Locate every blood parasite and identify its species.
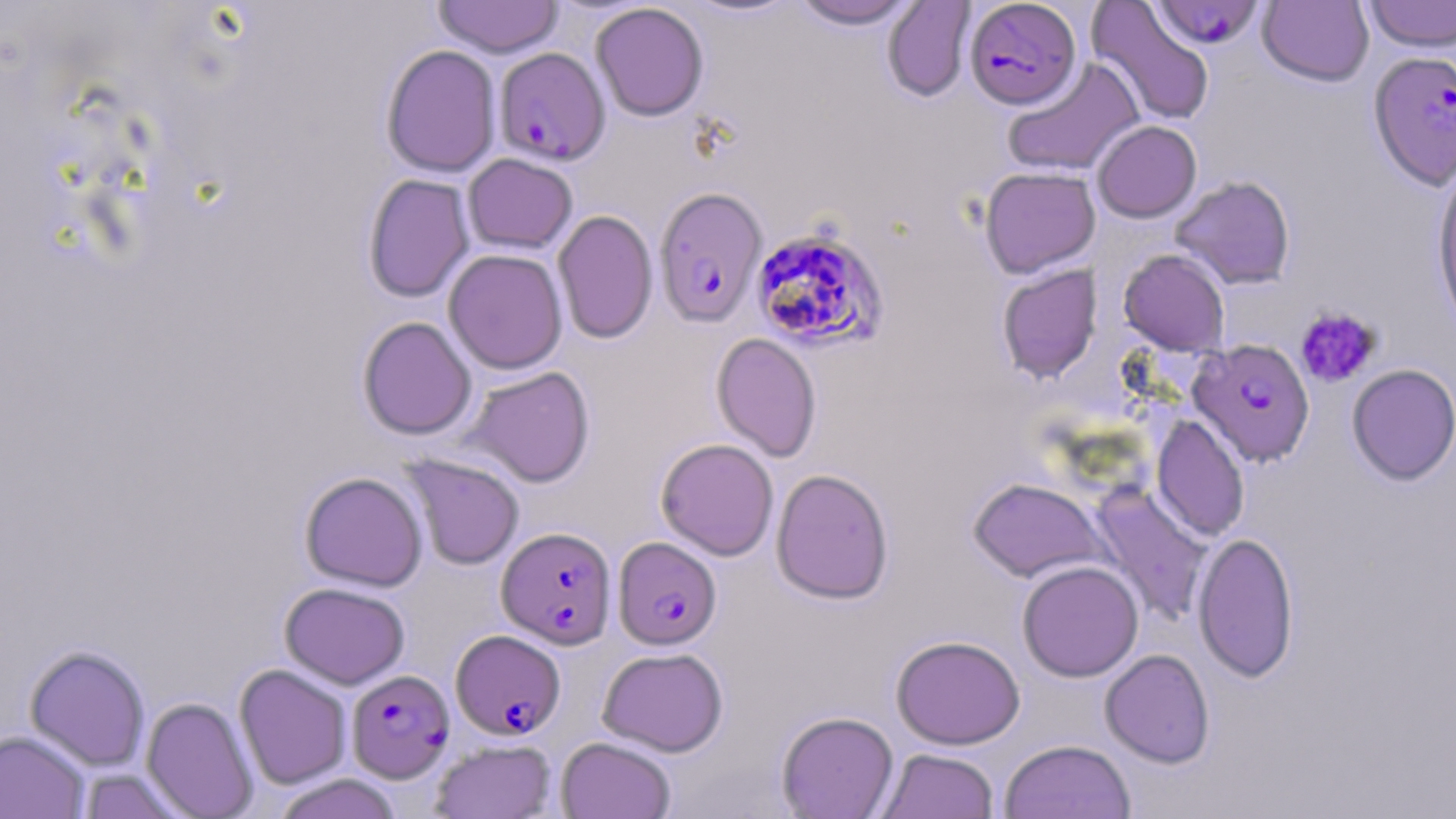
Approximate bounding boxes as [x1, y1, x2, y2] in pixels.
Plasmodium falciparum-infected red blood cells: [965, 0, 1081, 109], [1151, 1, 1264, 48], [494, 47, 610, 166], [1368, 50, 1456, 191], [653, 186, 768, 328], [751, 228, 888, 352], [1189, 338, 1315, 467], [497, 526, 617, 648], [613, 536, 721, 650], [450, 629, 565, 740], [346, 669, 454, 783].
No Plasmodium ovale, Plasmodium malariae, Plasmodium vivax, Babesia divergens, or Trypanosoma brucei observed.

Platelet locations: [1296, 306, 1382, 388]. Uninfected red blood cell locations: [678, 0, 806, 20], [790, 0, 920, 29], [1087, 0, 1215, 126], [1361, 0, 1456, 52], [433, 1, 564, 58], [881, 1, 976, 102], [1258, 1, 1374, 87], [590, 2, 709, 121], [380, 44, 502, 177], [1002, 57, 1144, 177], [1091, 120, 1202, 222], [462, 153, 578, 254], [1431, 165, 1456, 340], [979, 166, 1100, 278], [362, 173, 475, 303], [1170, 175, 1296, 290], [552, 209, 658, 345], [443, 249, 568, 374], [1118, 249, 1230, 355], [997, 264, 1102, 383], [357, 316, 477, 440], [711, 332, 822, 462], [1347, 364, 1456, 485], [465, 366, 595, 487], [1151, 414, 1250, 542], [655, 438, 779, 560], [400, 453, 525, 570], [771, 468, 894, 604], [299, 471, 428, 591], [968, 477, 1106, 583], [1089, 483, 1213, 626], [1193, 530, 1299, 683], [1017, 560, 1144, 682], [279, 582, 410, 689], [891, 634, 1025, 749], [24, 644, 150, 770], [598, 646, 728, 757], [1099, 648, 1215, 768], [234, 664, 352, 789], [141, 697, 258, 818], [776, 711, 899, 818], [0, 729, 90, 818], [556, 736, 675, 819], [430, 738, 557, 819], [999, 739, 1137, 819], [876, 748, 1000, 819], [76, 767, 190, 818], [273, 774, 402, 819]. Slide-level diagnosis: Plasmodium falciparum. Captured at 1000x magnification. Image is 1456×819 pixels. Thin blood smear. Optical microscopy. May-Grünwald-Giemsa-stained preparation. One field of a larger specimen.